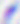
400x magnification. Toxoplasma gondii is seen. Photomicrograph.